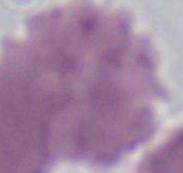
A red blood cell is shown. 1000x magnification. Micrograph.